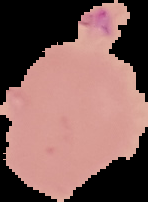
result = no Plasmodium parasites seen
image size = 148×202 pixels
preparation = thin blood film
image type = segmented cell region with the area outside set to black